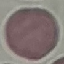

Result: no malaria parasites detected. Giemsa stain. Cell patch, automatically extracted from a larger field of view and resized to 64 × 64 pixels. Acquired by smartphone through the microscope eyepiece. Thin blood smear.